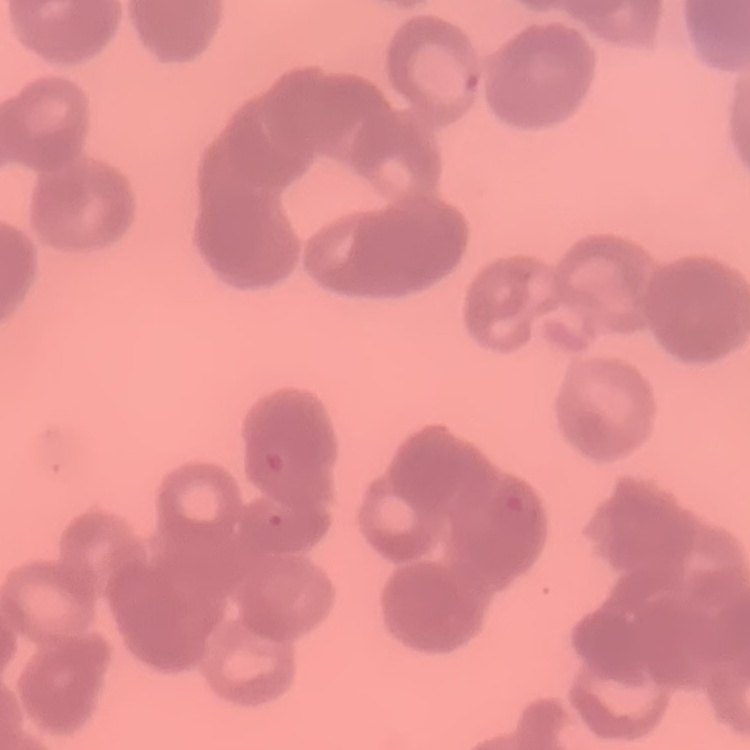 The red blood cells exhibit rouleaux formation. Field's or Giemsa stain. Square crop of a larger photomicrograph. Thin peripheral smear.